Report the malaria status of this cell.
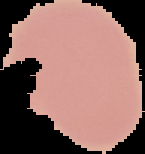

Uninfected.

Summary:
  - Preparation: thin blood smear
  - Image size: 145×154 pixels
  - Image type: segmented cell region with the area outside set to black